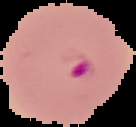
preparation = thin blood film
image type = segmented cell region on a black background
malaria status = parasitized
image size = 136×127 pixels